Locate every malaria parasite.
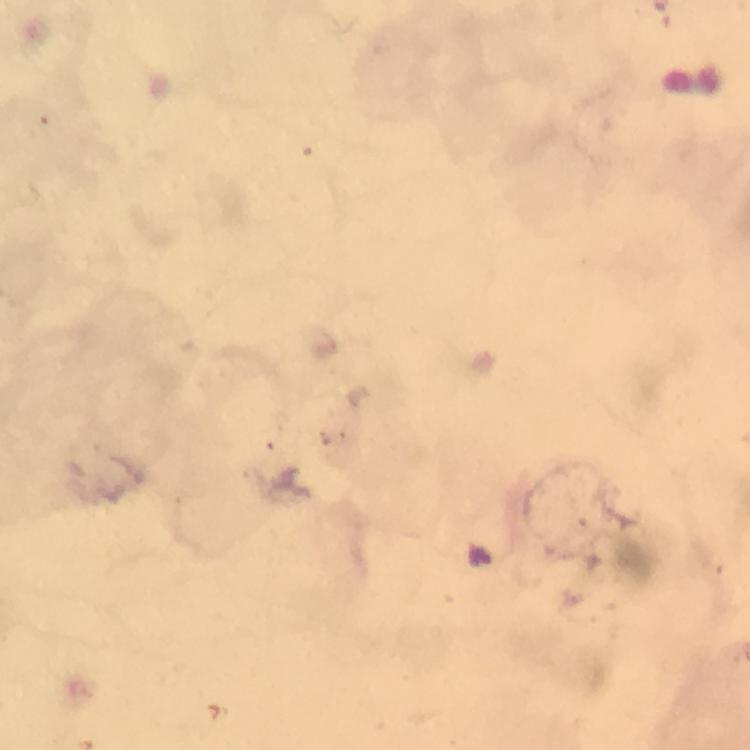
Approximate centers as [x, y] in pixels.
Malaria parasites: [481, 557].

A crop from one field of view. Thick blood film. 100x magnification. Photographed with a smartphone mounted on the microscope. Giemsa stain. Image is 750×750 pixels. From a malaria diagnostic workup. Immersion oil applied.